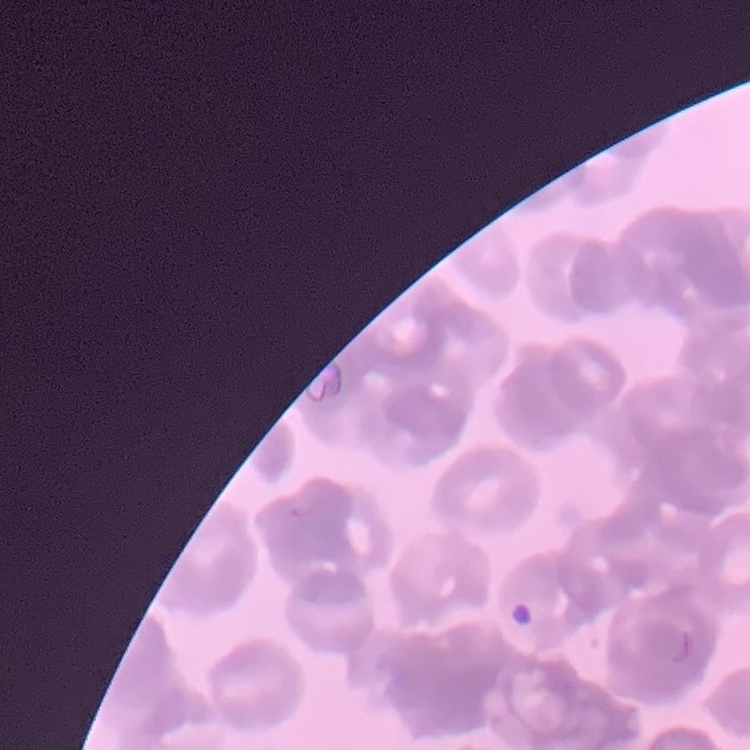

Summary:
  - Red blood cell morphology: rouleaux formation
  - Stain: Field's or Giemsa
  - Image type: one tile cut from a larger photomicrograph
  - Preparation: thin blood film